Classify this cell by malaria status.
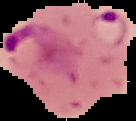

Parasitized.

Summary:
  - Image type: cell region segmented out of the field of view; surrounding area masked to black
  - Preparation: thin blood smear
  - Image size: 136×121 pixels